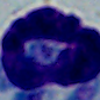

magnification: 1000x
identification: leukocyte
modality: photomicrograph